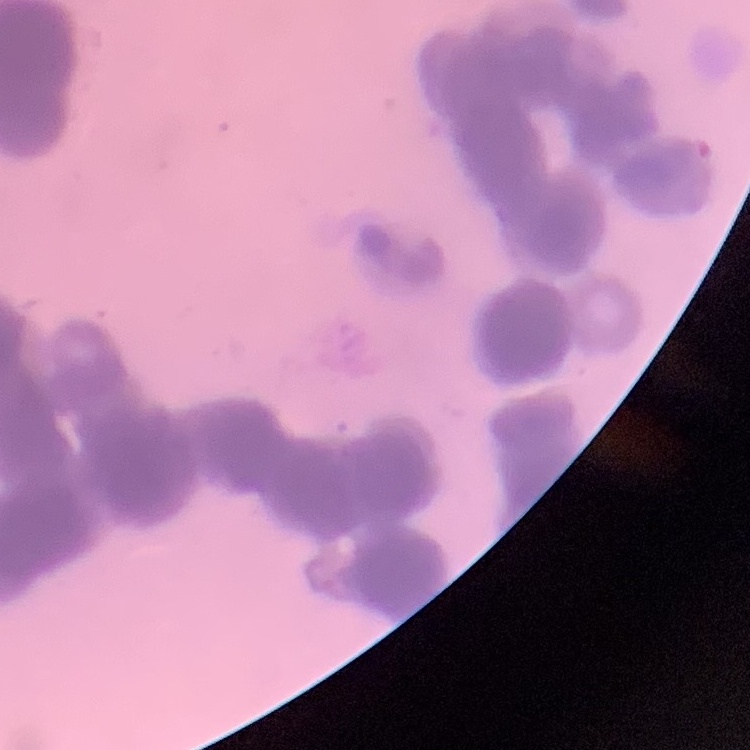
Summary:
  - Erythrocyte morphology: rouleaux formation
  - Image type: square crop of a larger photomicrograph
  - Preparation: thin blood smear
  - Stain: Field's or Giemsa